Identify the preparation type.
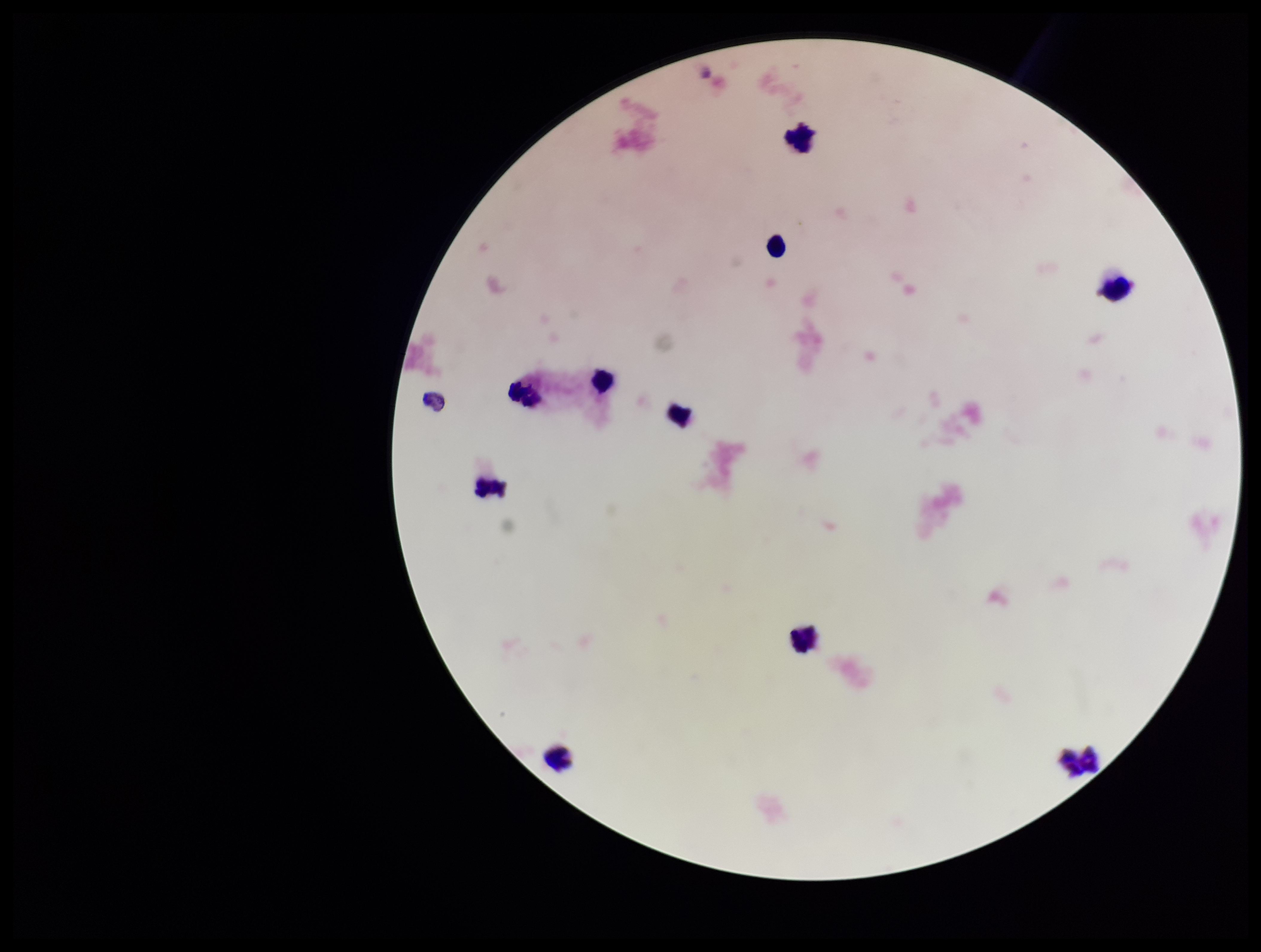
It is a thick blood smear.

stain = Giemsa
Plasmodium parasites = none identified
parasite count = 0
leukocyte count = 10
image size = 1261×952 pixels
field of view = one from this slide
patient malaria status = negative
capture = smartphone photograph through the microscope eyepiece